Identify the cell.
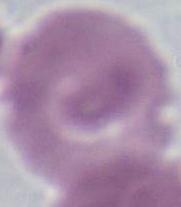
This is an erythrocyte.

Summary:
  - Modality: photomicrograph
  - Magnification: 1000x